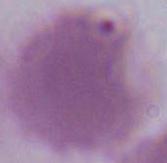

Summary:
  - Modality: micrograph
  - Magnification: 1000x
  - Identification: red blood cell